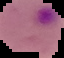
malaria_status: parasitized
image_size: 64×58 pixels
preparation: thin blood film
image_type: segmented cell region with the area outside set to black